Assess this cell for malaria.
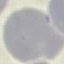
Uninfected.

Cell patch, automatically extracted from a larger field of view and resized to 64 × 64 pixels. Thin smear of blood. Photographed with a smartphone camera at the microscope eyepiece. Giemsa stain.